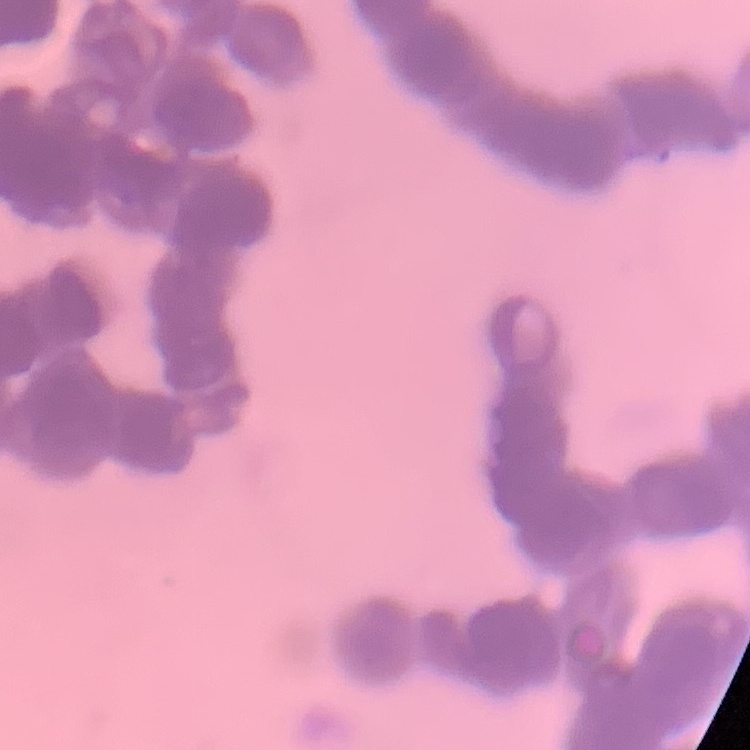
erythrocyte morphology = rouleaux formation
stain = Field's or Giemsa
image type = square crop of a larger photomicrograph
preparation = thin blood film